State which parasite is depicted.
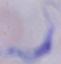

A trypanosome.

Summary:
  - Magnification: 1000x
  - Modality: photomicrograph